Locate every Trypanosoma brucei.
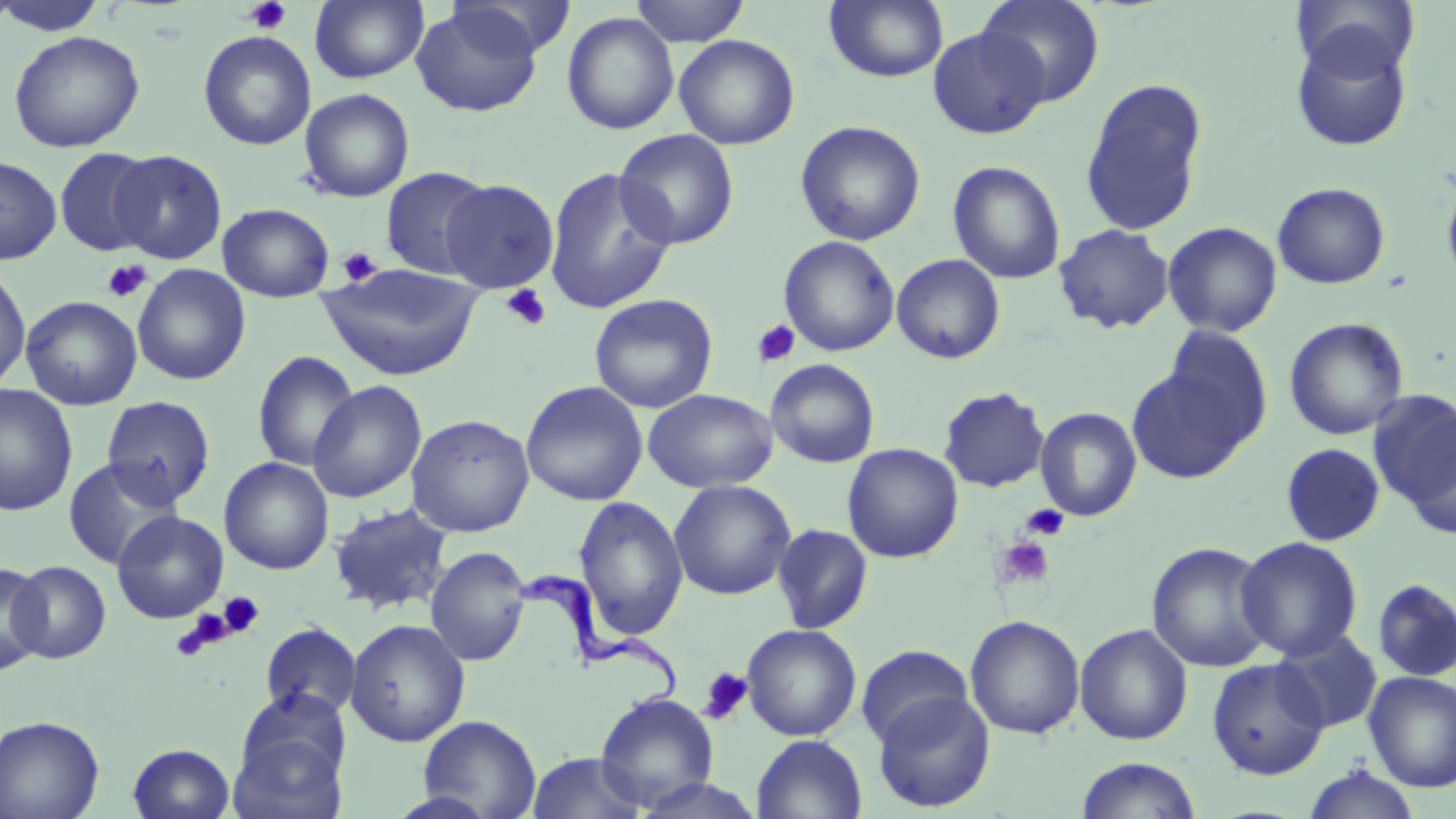
Approximate bounding boxes as (x1,y1)-(x2,y2) corner pairs in pixels.
Trypanosoma brucei: (516,569)-(683,714).

Summary:
  - Platelet locations: (241,0)-(291,35), (338,246)-(383,286), (102,259)-(152,302), (501,284)-(552,332), (753,319)-(801,367), (1021,504)-(1070,541), (993,535)-(1056,591), (219,592)-(264,638), (171,613)-(229,660), (698,666)-(753,725)
  - Uninfected red blood cell locations: (1,0)-(108,36), (309,0)-(429,84), (630,0)-(750,46), (823,0)-(949,83), (978,0)-(1106,106), (1292,0)-(1420,80), (447,1)-(575,59), (410,4)-(544,117), (561,12)-(680,135), (927,26)-(1050,139), (1290,28)-(1414,152), (7,30)-(145,153), (198,30)-(317,151), (674,34)-(800,150), (1080,77)-(1209,237), (299,88)-(415,202), (794,120)-(926,246), (614,128)-(739,250), (54,147)-(157,257), (110,149)-(227,264), (0,155)-(62,265), (948,160)-(1066,285), (380,165)-(494,280), (544,166)-(677,315), (1441,177)-(1456,292), (440,178)-(560,292), (1272,182)-(1391,289), (218,203)-(335,302), (1163,221)-(1283,337), (1053,223)-(1175,334), (778,235)-(900,357), (892,254)-(1006,364), (316,263)-(485,382), (0,264)-(31,393), (132,264)-(251,386), (589,294)-(718,413), (21,295)-(142,411), (1283,317)-(1409,440), (1163,326)-(1273,445), (252,349)-(360,472), (766,359)-(880,468), (1126,365)-(1253,483), (308,380)-(427,504), (520,380)-(649,506), (0,384)-(78,516), (938,387)-(1050,493), (643,389)-(777,493), (1372,391)-(1456,534), (101,395)-(216,507), (1035,407)-(1142,521), (406,414)-(535,537), (1281,442)-(1386,546), (842,443)-(964,563), (218,456)-(335,575), (63,457)-(183,570), (668,479)-(797,600), (573,495)-(689,641), (327,503)-(454,617), (111,510)-(229,623), (771,524)-(874,634), (1236,536)-(1363,661), (1147,541)-(1274,672), (425,546)-(531,667), (1,560)-(49,675), (7,561)-(112,663), (1372,579)-(1456,682), (965,614)-(1086,739), (345,618)-(470,747), (260,622)-(362,719), (1074,623)-(1193,745), (741,624)-(862,741), (1272,630)-(1383,733), (855,644)-(974,749), (1207,658)-(1330,779), (1363,671)-(1456,792), (872,690)-(996,813), (595,691)-(719,811), (230,694)-(351,816), (417,714)-(541,818), (0,715)-(105,819), (751,734)-(867,819), (128,743)-(235,819), (525,750)-(648,819), (1074,757)-(1202,819), (1302,765)-(1422,819), (632,777)-(769,819)
  - Slide-level diagnosis: Trypanosoma brucei
  - Preparation: thin blood smear
  - Magnification: 1000x
  - Field of view: one of a larger specimen
  - Stain: May-Grünwald-Giemsa
  - Modality: light microscopy
  - Image size: 1456×819 pixels